Describe the morphology of the red blood cells.
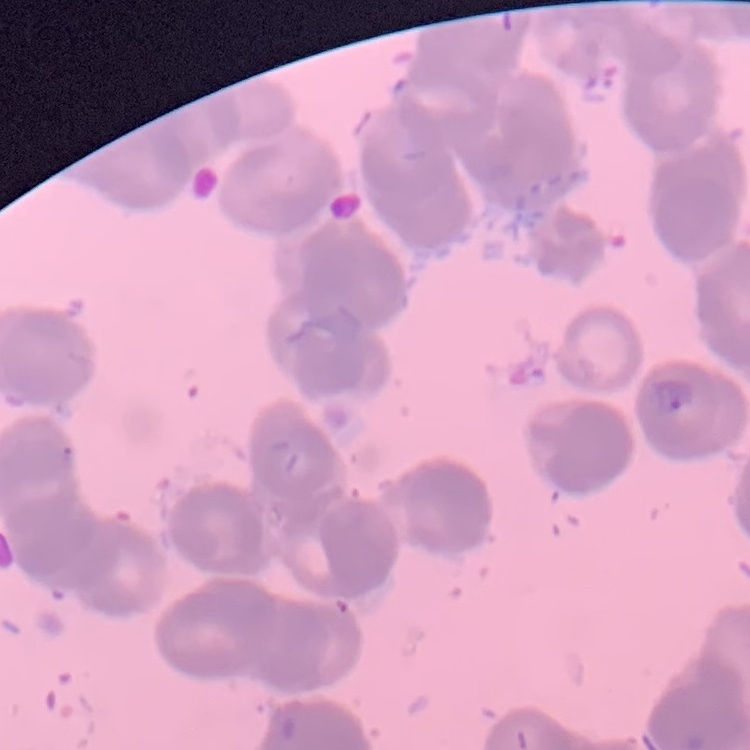
They show rouleaux formation.

image type = square crop of a larger photomicrograph
preparation = thin blood smear
stain = Field's or Giemsa